Describe the morphology of the red blood cells.
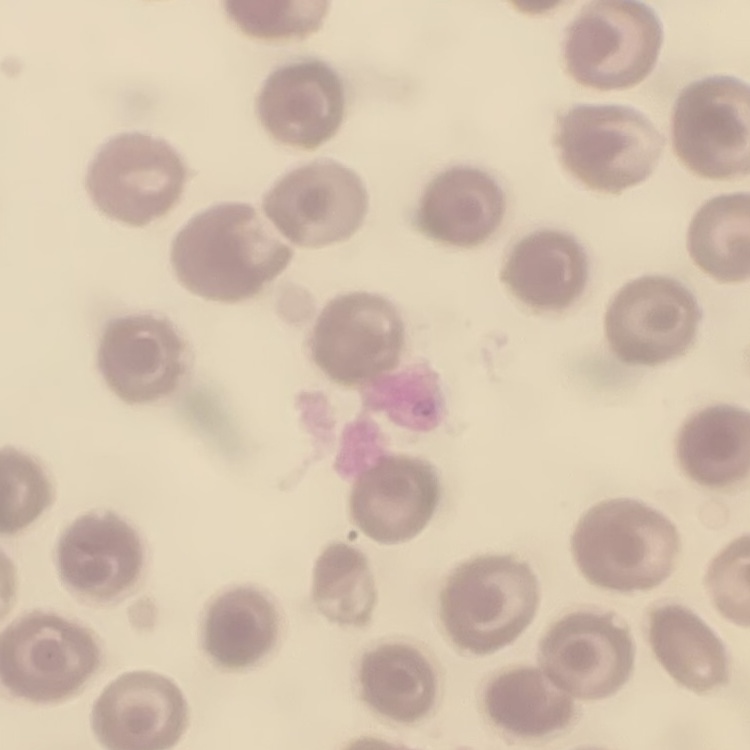
They show no rouleaux formation.

Summary:
  - Stain: Field's or Giemsa
  - Image type: one tile cut from a larger photomicrograph
  - Preparation: thin blood smear